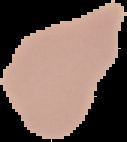 From a thin blood film. Malaria status: uninfected. Image is 127×142 pixels. Segmented cell region on a black background.